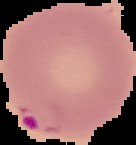
Image is 136×145 pixels. Result: malaria parasites detected. Cell region segmented out of the field of view; the surrounding area is masked to black. From a thin blood smear.